Comment on the background quality.
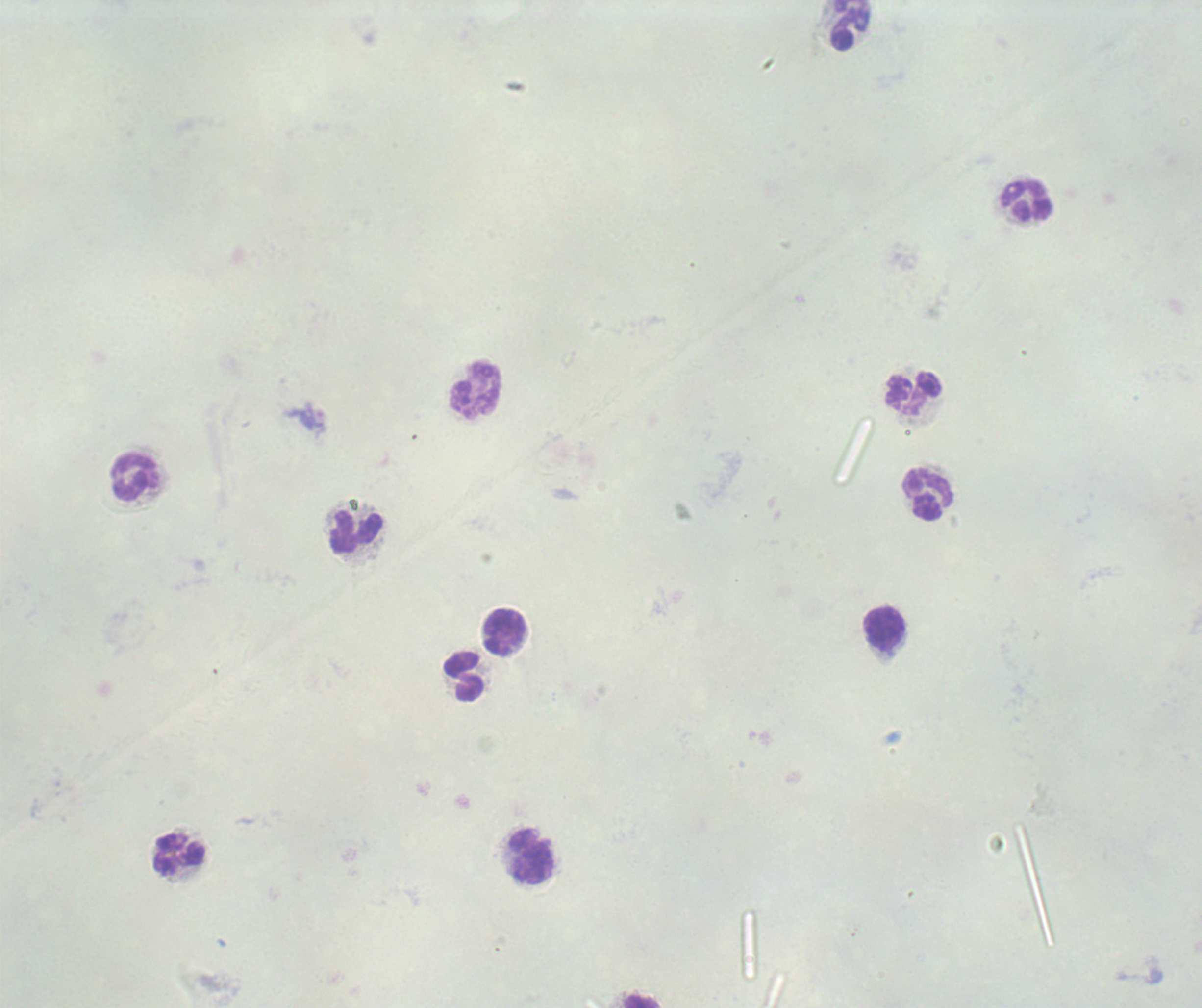
It is poor.

result: no Plasmodium parasites seen
image_size: 1202×1008 pixels
stain: Romanowsky
field_of_view: one from this slide
preparation: thick blood smear
magnification: 100x
context: previously used in a real diagnosis
leukocyte_locations: 'approximate centers as (x, y) in pixels: (851, 25), (1027, 202), (475, 390), (914, 395), (136, 477), (927, 495), (355, 532), (884, 630), (505, 631), (464, 676), (180, 855), (532, 857)'